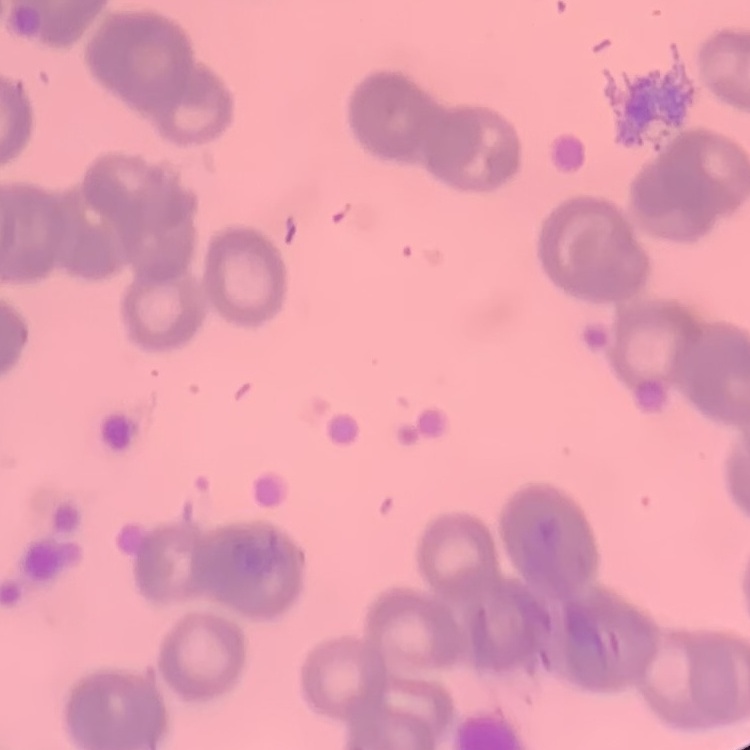

red blood cell morphology = rouleaux formation
stain = Field's or Giemsa
preparation = thin blood film
image type = one tile cut from a larger photomicrograph